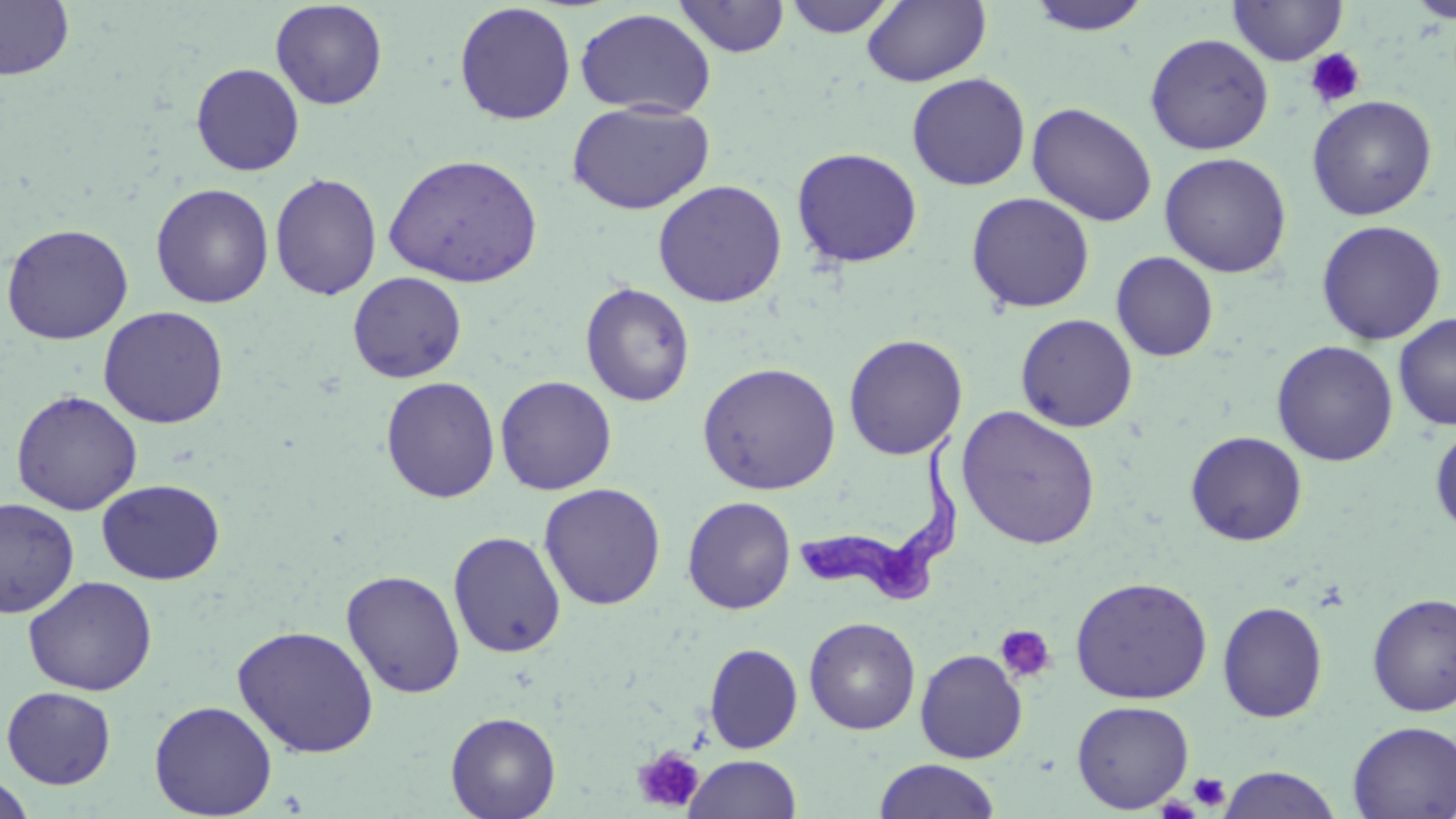

Summary:
  - Coordinate format: approximate bounding boxes as named x1/y1/x2/y2 corners in pixels
  - Platelet locations: (x1=1304, y1=48, x2=1365, y2=108), (x1=994, y1=625, x2=1056, y2=684), (x1=632, y1=746, x2=705, y2=813), (x1=1189, y1=772, x2=1230, y2=811)
  - Trypanosoma brucei locations: (x1=784, y1=421, x2=963, y2=614)
  - Uninfected red blood cell locations: (x1=673, y1=0, x2=790, y2=58), (x1=783, y1=0, x2=899, y2=38), (x1=862, y1=0, x2=991, y2=87), (x1=1025, y1=0, x2=1153, y2=36), (x1=1407, y1=0, x2=1456, y2=23), (x1=0, y1=1, x2=75, y2=81), (x1=270, y1=1, x2=388, y2=110), (x1=1228, y1=1, x2=1348, y2=66), (x1=453, y1=2, x2=577, y2=125), (x1=575, y1=7, x2=716, y2=118), (x1=1144, y1=33, x2=1274, y2=155), (x1=190, y1=63, x2=305, y2=176), (x1=906, y1=72, x2=1031, y2=191), (x1=1306, y1=95, x2=1438, y2=221), (x1=566, y1=100, x2=716, y2=216), (x1=1027, y1=102, x2=1158, y2=227), (x1=791, y1=147, x2=923, y2=268), (x1=383, y1=152, x2=544, y2=288), (x1=1159, y1=152, x2=1292, y2=277), (x1=269, y1=172, x2=382, y2=301), (x1=652, y1=179, x2=787, y2=308), (x1=150, y1=183, x2=274, y2=309), (x1=966, y1=192, x2=1095, y2=313), (x1=1315, y1=220, x2=1447, y2=346), (x1=0, y1=222, x2=134, y2=344), (x1=1111, y1=252, x2=1219, y2=362), (x1=347, y1=271, x2=467, y2=383), (x1=580, y1=282, x2=695, y2=407), (x1=98, y1=305, x2=229, y2=429), (x1=1393, y1=312, x2=1456, y2=431), (x1=1015, y1=313, x2=1138, y2=432), (x1=843, y1=334, x2=968, y2=459), (x1=1271, y1=340, x2=1398, y2=467), (x1=697, y1=361, x2=841, y2=495), (x1=495, y1=375, x2=617, y2=495), (x1=381, y1=376, x2=501, y2=503), (x1=11, y1=390, x2=143, y2=515), (x1=956, y1=405, x2=1101, y2=550), (x1=1430, y1=421, x2=1456, y2=537), (x1=1185, y1=431, x2=1307, y2=546), (x1=97, y1=479, x2=225, y2=585), (x1=538, y1=482, x2=667, y2=610), (x1=682, y1=496, x2=796, y2=614), (x1=0, y1=498, x2=79, y2=618), (x1=448, y1=530, x2=566, y2=658), (x1=341, y1=569, x2=466, y2=699), (x1=23, y1=575, x2=158, y2=696), (x1=1069, y1=576, x2=1213, y2=705), (x1=1366, y1=592, x2=1456, y2=717), (x1=1216, y1=601, x2=1329, y2=723), (x1=804, y1=616, x2=921, y2=735), (x1=232, y1=625, x2=380, y2=758), (x1=704, y1=643, x2=803, y2=753), (x1=914, y1=649, x2=1028, y2=763), (x1=2, y1=686, x2=117, y2=788), (x1=149, y1=700, x2=278, y2=818), (x1=1071, y1=700, x2=1195, y2=813), (x1=445, y1=711, x2=561, y2=819), (x1=1347, y1=720, x2=1456, y2=818), (x1=683, y1=754, x2=802, y2=819), (x1=874, y1=759, x2=1001, y2=818), (x1=1217, y1=766, x2=1344, y2=819), (x1=0, y1=773, x2=36, y2=818)
  - Slide-level diagnosis: Trypanosoma brucei
  - Stain: May-Grünwald-Giemsa
  - Preparation: thin blood smear
  - Field of view: single
  - Image size: 1456×819 pixels
  - Modality: light microscopy
  - Magnification: 1000x